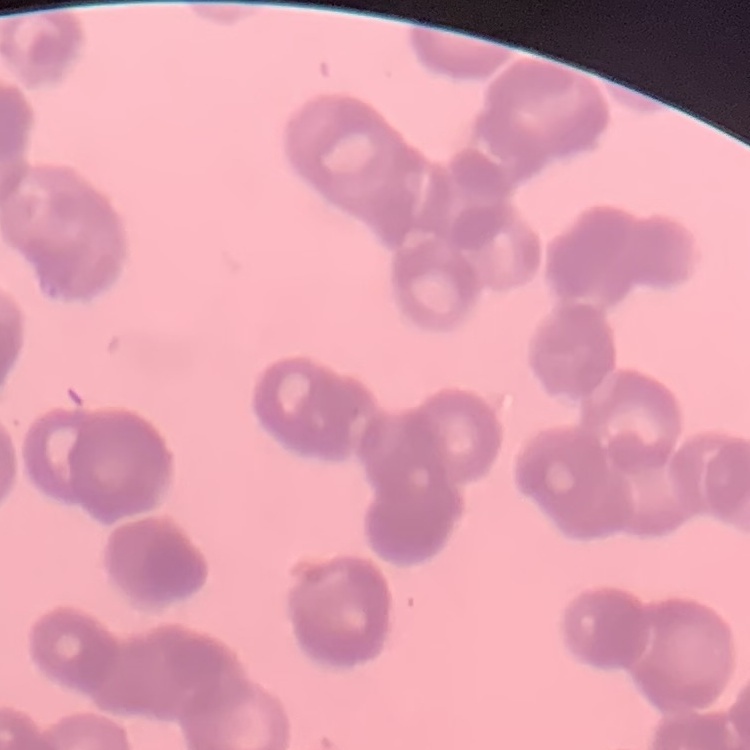

Summary:
  - Red blood cell morphology: rouleaux formation
  - Preparation: thin peripheral smear
  - Image type: one tile cut from a larger photomicrograph
  - Stain: Field's or Giemsa